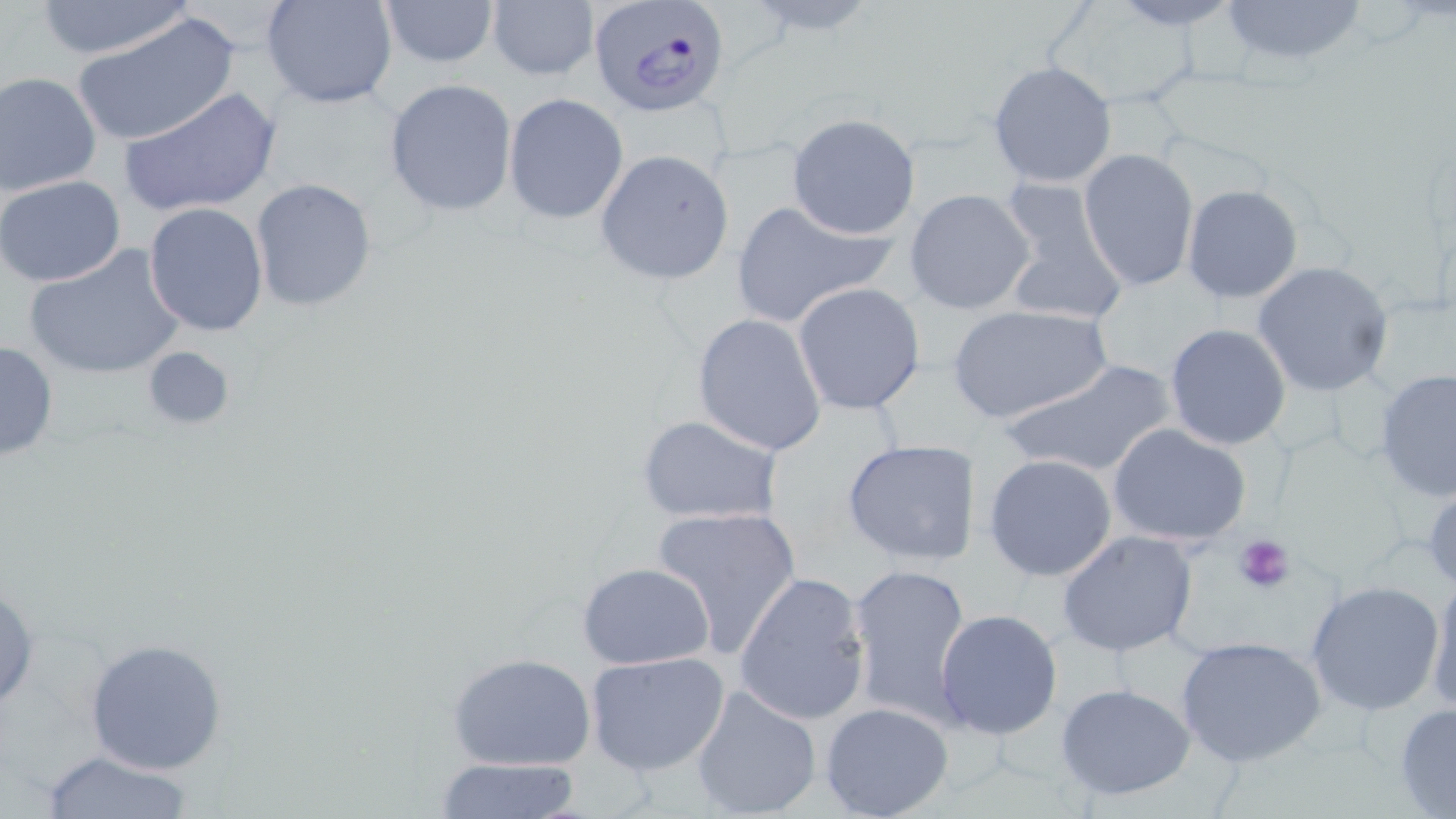
Approximate bounding boxes as named x1/y1/x2/y2 corners in pixels. Uninfected red blood cell locations: (x1=32, y1=0, x2=199, y2=60), (x1=261, y1=0, x2=400, y2=110), (x1=378, y1=0, x2=498, y2=67), (x1=484, y1=0, x2=597, y2=82), (x1=1217, y1=0, x2=1369, y2=69), (x1=1047, y1=2, x2=1199, y2=108), (x1=69, y1=13, x2=241, y2=151), (x1=987, y1=60, x2=1117, y2=189), (x1=0, y1=71, x2=102, y2=197), (x1=383, y1=78, x2=518, y2=216), (x1=121, y1=86, x2=281, y2=219), (x1=504, y1=92, x2=629, y2=224), (x1=786, y1=113, x2=921, y2=240), (x1=1078, y1=148, x2=1199, y2=291), (x1=595, y1=150, x2=734, y2=285), (x1=1, y1=175, x2=126, y2=288), (x1=994, y1=177, x2=1130, y2=328), (x1=251, y1=180, x2=378, y2=311), (x1=1180, y1=184, x2=1305, y2=304), (x1=905, y1=188, x2=1036, y2=315), (x1=727, y1=197, x2=894, y2=328), (x1=143, y1=201, x2=269, y2=336), (x1=24, y1=243, x2=187, y2=381), (x1=1252, y1=261, x2=1396, y2=397), (x1=794, y1=281, x2=925, y2=416), (x1=947, y1=305, x2=1111, y2=427), (x1=691, y1=313, x2=827, y2=455), (x1=1164, y1=324, x2=1292, y2=449), (x1=0, y1=339, x2=59, y2=463), (x1=140, y1=345, x2=237, y2=432), (x1=1001, y1=358, x2=1178, y2=481), (x1=1375, y1=369, x2=1456, y2=502), (x1=637, y1=415, x2=784, y2=525), (x1=1107, y1=422, x2=1252, y2=547), (x1=841, y1=439, x2=980, y2=567), (x1=981, y1=453, x2=1119, y2=582), (x1=1423, y1=475, x2=1456, y2=595), (x1=652, y1=506, x2=803, y2=660), (x1=1055, y1=530, x2=1200, y2=657), (x1=847, y1=560, x2=972, y2=724), (x1=576, y1=562, x2=715, y2=670), (x1=733, y1=570, x2=871, y2=725), (x1=1426, y1=574, x2=1456, y2=717), (x1=0, y1=579, x2=39, y2=714), (x1=1303, y1=581, x2=1445, y2=717), (x1=934, y1=608, x2=1063, y2=741), (x1=1174, y1=635, x2=1326, y2=766), (x1=84, y1=637, x2=229, y2=775), (x1=448, y1=651, x2=598, y2=772), (x1=583, y1=651, x2=730, y2=777), (x1=1055, y1=682, x2=1199, y2=802), (x1=690, y1=684, x2=823, y2=819), (x1=1393, y1=702, x2=1456, y2=818), (x1=820, y1=703, x2=954, y2=819), (x1=39, y1=747, x2=195, y2=818), (x1=431, y1=756, x2=585, y2=819). Plasmodium falciparum-infected red blood cell locations: (x1=585, y1=0, x2=731, y2=119). Platelet locations: (x1=1235, y1=534, x2=1296, y2=593). Slide-level diagnosis: Plasmodium falciparum. Optical microscopy. Thin blood film. Image is 1456×819 pixels. Captured at 1000x magnification. Single field of view. May-Grünwald-Giemsa-stained preparation.